Locate every Plasmodium falciparum-infected red blood cell.
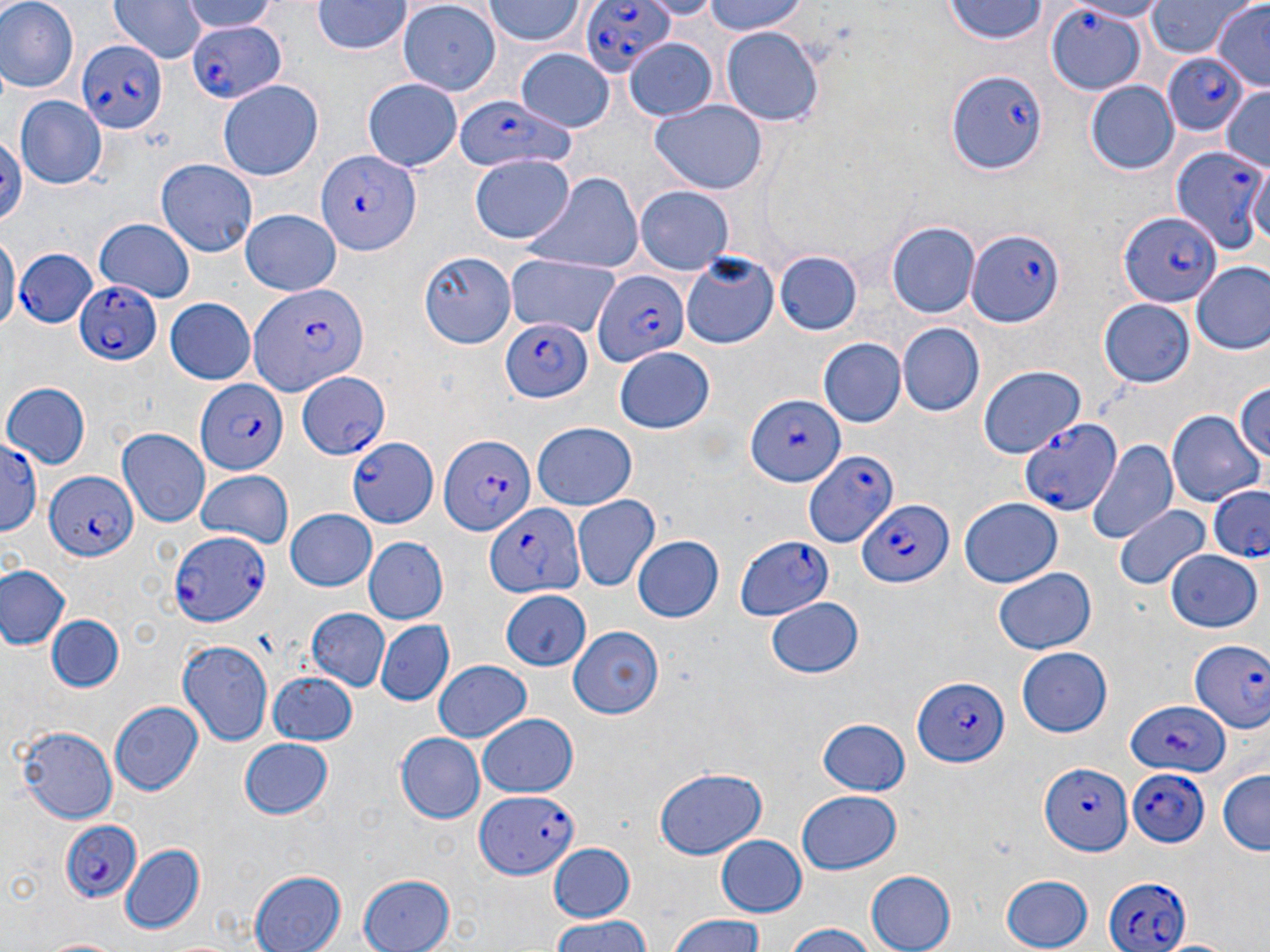
Approximate bounding boxes as [x1, y1, x2, y2] in pixels.
Plasmodium falciparum-infected red blood cells (subset): [579, 0, 673, 81], [1047, 6, 1150, 97], [186, 17, 284, 106], [76, 41, 164, 135], [1160, 53, 1250, 135], [948, 69, 1045, 173], [448, 92, 576, 178], [1169, 143, 1266, 258], [319, 145, 427, 252], [1121, 212, 1219, 309], [967, 227, 1064, 326], [11, 246, 102, 333], [593, 269, 689, 368], [72, 280, 163, 366], [249, 280, 365, 393], [501, 317, 591, 401], [296, 369, 392, 465], [196, 379, 290, 477], [745, 392, 848, 487], [1021, 418, 1121, 516], [438, 433, 535, 539], [0, 435, 41, 541], [346, 435, 440, 530], [800, 442, 893, 553], [44, 472, 136, 563], [1208, 486, 1269, 560], [861, 495, 953, 588], [482, 502, 584, 602], [168, 530, 269, 626], [1186, 632, 1270, 740], [912, 678, 1007, 767], [1125, 700, 1228, 776], [1040, 764, 1135, 856], [1124, 767, 1210, 847], [476, 791, 576, 881], [57, 820, 145, 903], [1104, 872, 1191, 952].

Uninfected red blood cell locations (subset): [0, 0, 78, 93], [108, 0, 204, 65], [182, 0, 280, 32], [702, 0, 813, 37], [1066, 0, 1172, 21], [1146, 0, 1250, 60], [312, 1, 411, 56], [482, 1, 588, 47], [943, 2, 1049, 47], [396, 3, 501, 97], [1211, 3, 1270, 90], [721, 25, 823, 125], [623, 35, 718, 121], [515, 47, 615, 130], [1086, 78, 1180, 173], [360, 79, 464, 171], [218, 80, 324, 181], [1220, 84, 1270, 169], [16, 97, 106, 187], [650, 99, 768, 194], [0, 130, 27, 232], [471, 154, 574, 243], [1248, 158, 1270, 255], [157, 160, 257, 257], [520, 173, 643, 278], [637, 185, 735, 274], [240, 209, 341, 297], [95, 219, 194, 303], [886, 222, 978, 319], [0, 232, 17, 337], [420, 249, 517, 348], [775, 250, 861, 335], [681, 253, 780, 348], [507, 254, 622, 337], [1189, 260, 1270, 355], [165, 297, 256, 383], [1098, 298, 1197, 390], [898, 321, 985, 417], [819, 338, 906, 426], [614, 348, 716, 434], [980, 365, 1087, 459], [1231, 378, 1269, 471], [3, 382, 90, 467], [1209, 387, 1270, 501], [1167, 407, 1263, 506], [532, 421, 636, 510], [117, 428, 210, 524], [1084, 437, 1178, 545], [195, 470, 293, 548], [572, 496, 660, 591], [960, 498, 1063, 587], [1116, 504, 1209, 592], [284, 510, 376, 592], [736, 535, 835, 620], [361, 537, 449, 625], [633, 537, 722, 621], [1167, 548, 1264, 631], [0, 564, 71, 651], [994, 568, 1097, 655], [766, 597, 865, 680], [306, 607, 390, 690], [48, 614, 124, 692], [376, 620, 454, 707], [570, 626, 664, 718], [178, 638, 274, 750], [1016, 647, 1114, 737], [433, 660, 533, 743], [266, 668, 357, 745], [108, 700, 205, 796], [477, 713, 580, 798], [817, 714, 913, 795], [14, 725, 119, 824], [395, 733, 484, 823], [237, 738, 335, 821], [1216, 767, 1270, 857], [652, 768, 767, 861], [797, 792, 902, 875], [715, 835, 806, 916], [549, 842, 636, 925], [118, 843, 206, 934], [865, 869, 956, 952], [248, 870, 347, 952], [356, 871, 455, 952], [998, 873, 1094, 950], [668, 915, 768, 952], [548, 916, 655, 952], [781, 922, 882, 952], [39, 937, 123, 952]. Slide-level diagnosis: Plasmodium falciparum. One field of a larger specimen. Image is 1270×952 pixels. Thin blood smear. May-Grünwald-Giemsa stain. Light microscopy. 1000x magnification.